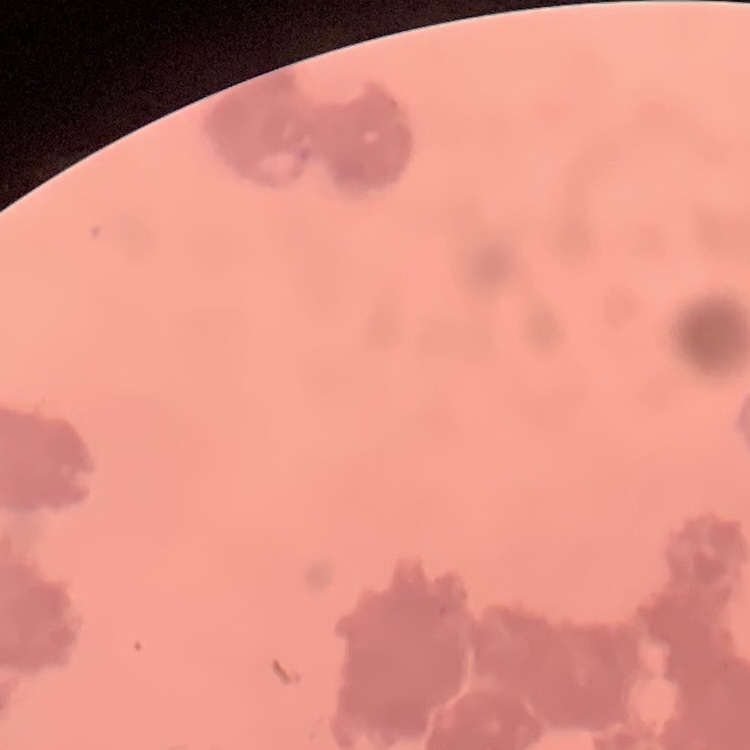

Summary:
  - Erythrocyte morphology: rouleaux formation
  - Preparation: thin blood film
  - Stain: Field's or Giemsa
  - Image type: square crop of a larger photomicrograph